Name the parasite shown.
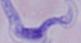

This is a trypanosome.

1000x magnification. Micrograph.